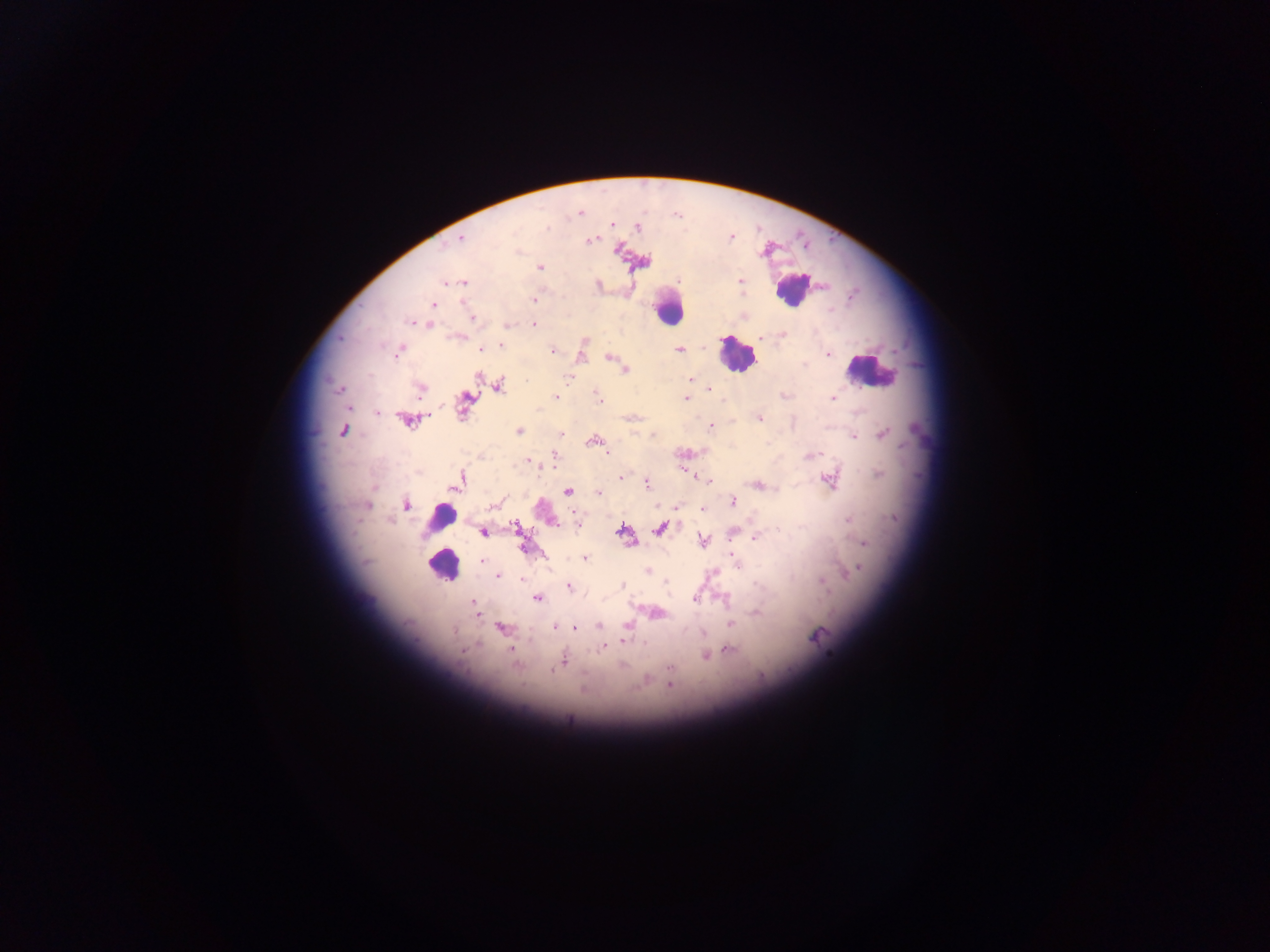

country = Ghana
field of view = single
preparation = thick blood smear
leukocyte locations = approximate centers as x y in pixels: 791 291; 668 310; 734 354; 871 371; 440 514; 442 566
image size = 1270×952 pixels
Plasmodium parasite locations = approximate centers as x y in pixels: 581 214; 677 215; 613 224; 639 227; 547 228; 731 236; 461 239; 590 240; 616 249; 540 267; 740 280; 677 281; 446 283; 463 283; 534 300; 433 304; 473 318; 409 322; 533 324; 429 325; 506 325; 783 334; 761 336; 584 342; 501 345; 702 346; 480 349; 679 350; 552 351; 397 352; 828 354; 609 357; 624 369; 478 376; 571 377; 691 379; 499 387; 338 388; 421 389; 707 389; 597 396; 556 397; 686 398; 833 398; 348 409; 377 412; 760 418; 409 421; 712 426; 343 430; 520 430; 561 434; 884 434; 653 436; 855 437; 607 453; 813 454; 555 455; 528 461; 621 478; 829 480; 458 482; 709 482; 647 483; 760 485; 568 492; 598 493; 733 502; 406 505; 368 506; 492 506; 657 506; 677 507; 702 509; 849 520; 517 526; 556 526; 577 526; 661 528; 622 531; 482 532; 756 537; 703 541; 864 543; 525 548; 733 557; 585 558; 482 560; 858 569; 647 571; 498 576; 522 578; 666 581; 822 581; 622 585; 568 587; 538 598; 725 598; 695 599; 473 602; 476 612; 756 612; 658 613; 730 625; 599 626; 501 627; 555 628; 574 628; 454 631; 704 633; 816 636; 623 641; 478 643; 644 643; 604 648; 511 649; 729 650; 464 651; 705 656; 563 661; 670 668; 556 669; 552 671; 670 684; 583 690
capture = mobile-phone photograph through a microscope